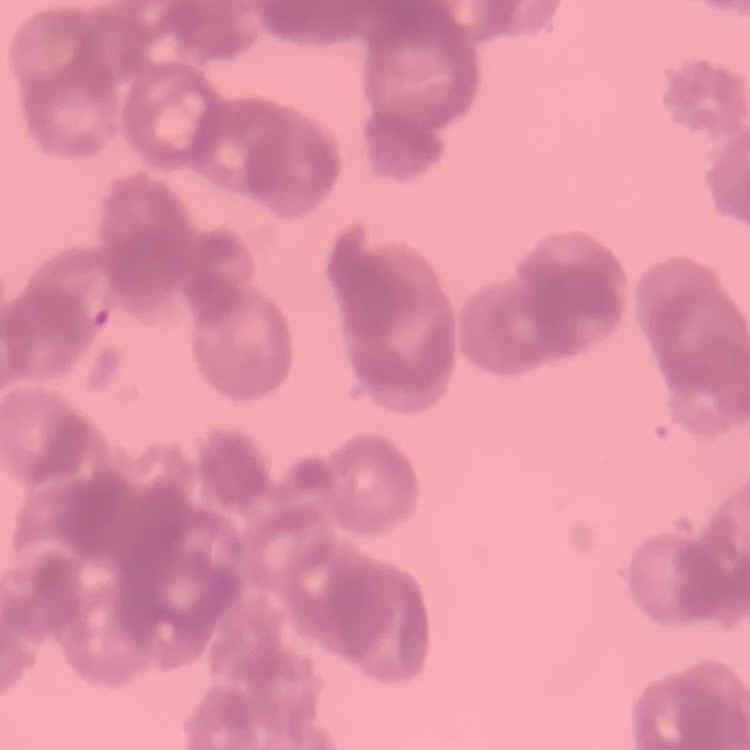

erythrocyte_morphology: rouleaux formation
stain: Field's or Giemsa
preparation: thin blood smear
image_type: one tile cut from a larger photomicrograph